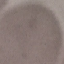
malaria status = uninfected
preparation = thin blood film
stain = Giemsa
image type = automatically extracted cell patch, resized to 64 × 64 pixels
capture = smartphone camera at the microscope eyepiece